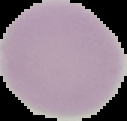
Image is 127×121 pixels. The area outside the segmented cell region is set to black. From a thin blood smear. Malaria status: uninfected.